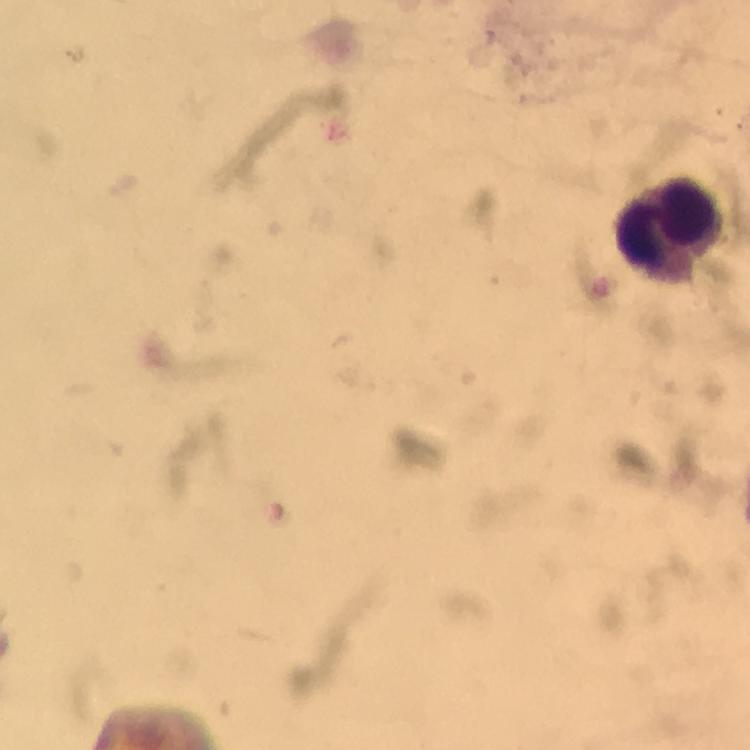

Approximate centers as [x, y] in pixels.
Summary:
  - Leukocyte locations: [672, 225]
  - Immersion oil: applied
  - Image size: 750×750 pixels
  - Context: from a malaria diagnostic workup
  - Malaria parasites: none detected
  - Magnification: 100x
  - Preparation: thick blood smear
  - Capture: smartphone camera through the microscope
  - Stain: Giemsa
  - Cropped from: a single field of view